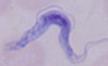

modality: photomicrograph
identification: trypanosome
magnification: 1000x